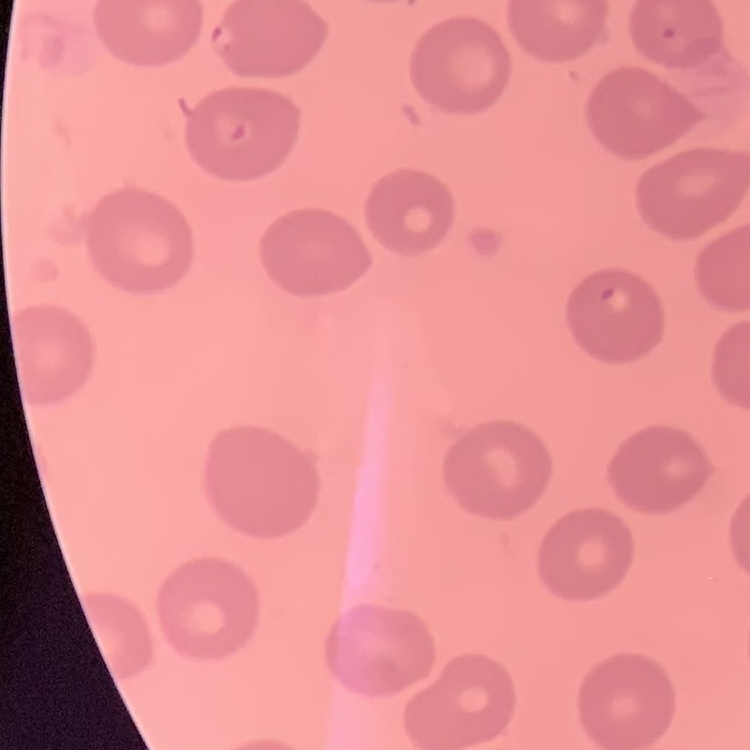

erythrocyte morphology = no rouleaux formation
image type = one tile cut from a larger photomicrograph
preparation = thin blood film
stain = Field's or Giemsa